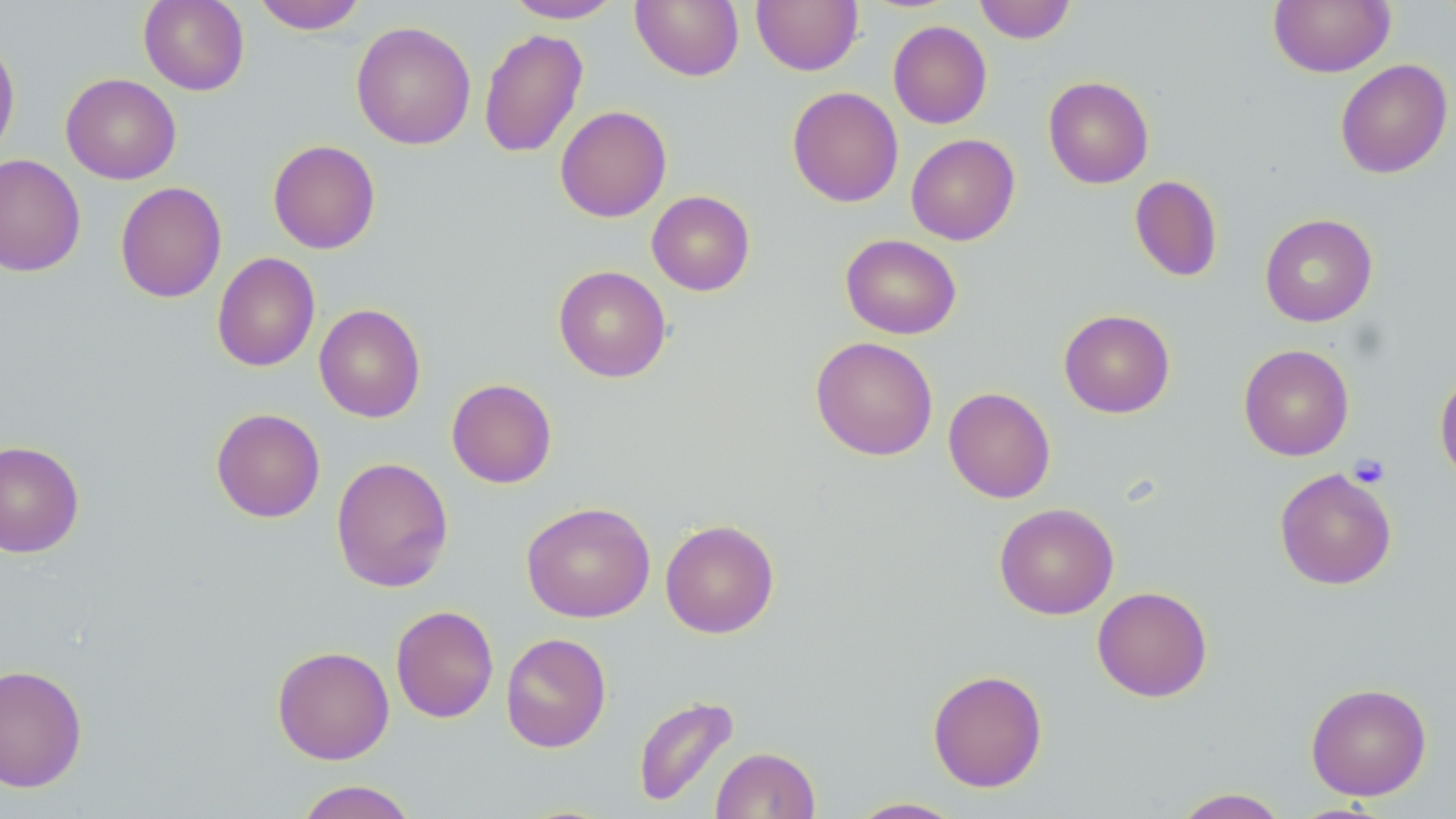
Summary:
  - Coordinate format: approximate bounding boxes as (x1, y1, x2, y2) in pixels
  - Uninfected red blood cell locations: (138, 0, 250, 95), (252, 0, 367, 34), (504, 0, 623, 23), (631, 0, 744, 81), (751, 0, 863, 75), (974, 0, 1076, 43), (1268, 0, 1395, 77), (351, 20, 476, 150), (888, 21, 992, 129), (478, 28, 588, 158), (0, 35, 20, 162), (1335, 59, 1453, 179), (61, 73, 182, 184), (1043, 76, 1154, 189), (787, 86, 903, 207), (555, 105, 672, 222), (906, 133, 1020, 245), (268, 139, 380, 254), (0, 153, 86, 277), (1129, 175, 1223, 282), (115, 181, 227, 303), (646, 190, 756, 295), (1259, 213, 1378, 326), (840, 233, 962, 339), (212, 252, 320, 372), (553, 265, 671, 382), (314, 303, 426, 423), (1059, 309, 1175, 418), (810, 336, 938, 461), (1238, 344, 1354, 460), (1434, 370, 1456, 486), (446, 378, 557, 489), (943, 386, 1056, 503), (211, 408, 325, 523), (0, 439, 84, 558), (331, 457, 454, 593), (1274, 468, 1397, 590), (521, 501, 655, 623), (994, 502, 1119, 620), (660, 519, 780, 638), (1092, 586, 1213, 702), (390, 605, 499, 723), (500, 632, 612, 753), (272, 645, 394, 764), (0, 663, 88, 793), (927, 669, 1048, 792), (1306, 682, 1432, 800), (631, 694, 740, 809), (711, 746, 820, 819), (293, 780, 419, 819), (1171, 787, 1292, 818), (847, 797, 966, 818)
  - Platelet locations: (1348, 454, 1390, 488)
  - Slide-level diagnosis: no evidence of blood parasites
  - Stain: May-Grünwald-Giemsa
  - Preparation: thin blood film
  - Modality: optical microscopy
  - Magnification: 1000x
  - Image size: 1456×819 pixels
  - Field of view: single